Point out each malaria parasite.
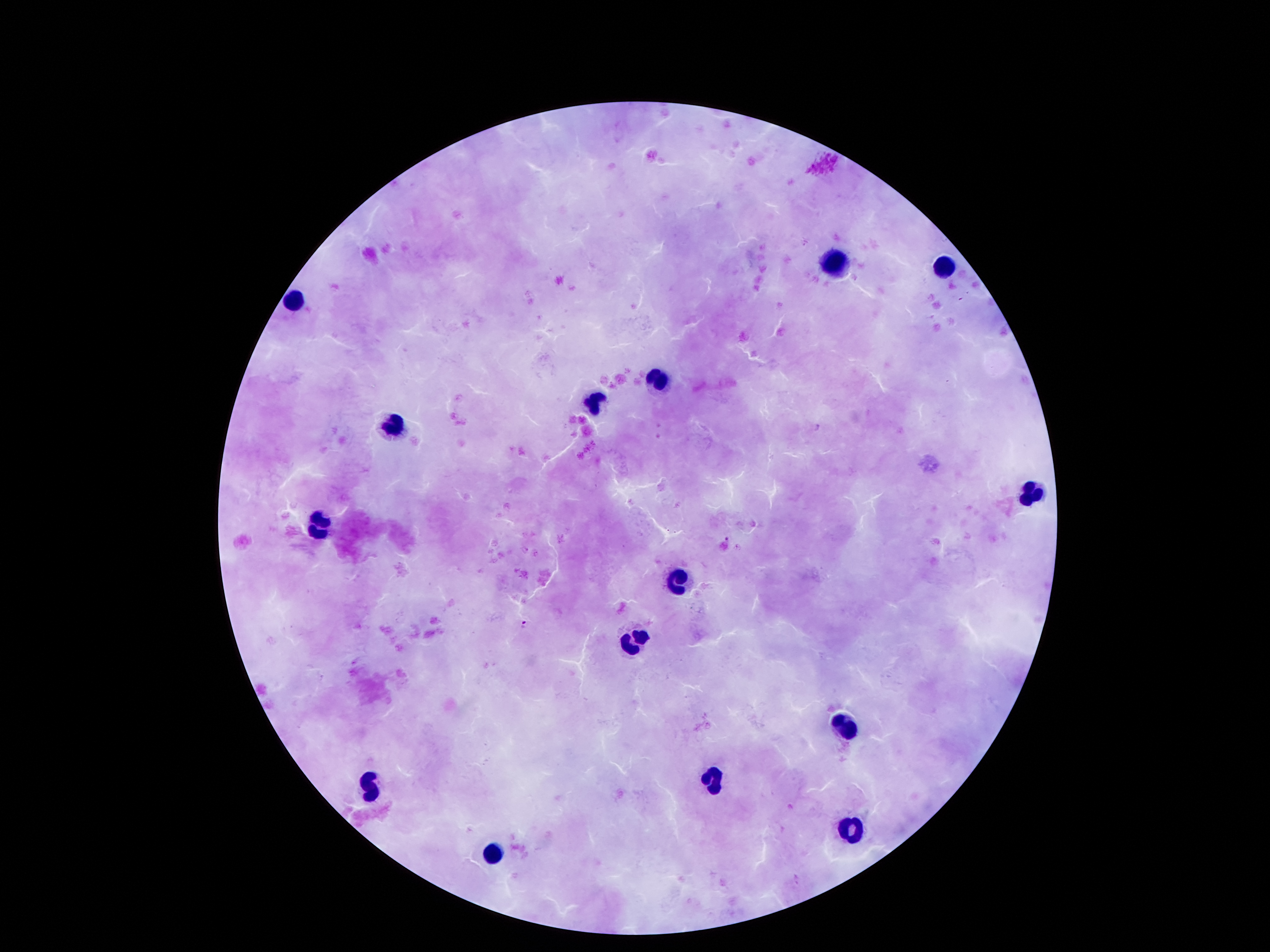
Approximate centers as {x, y} in pixels.
Malaria parasites: {818, 427}, {727, 539}, {524, 624}.

Summary:
  - Leukocyte locations: {832, 263}, {944, 267}, {293, 302}, {659, 382}, {594, 400}, {396, 430}, {1029, 493}, {322, 527}, {678, 580}, {633, 643}, {843, 727}, {716, 779}, {370, 791}, {854, 835}, {492, 855}
  - Capture: smartphone through the microscope eyepiece
  - Field of view: single
  - Patient malaria status: positive for Plasmodium falciparum
  - Preparation: thick blood smear
  - Image size: 1270×952 pixels
  - Magnification: 100x
  - Stain: Giemsa